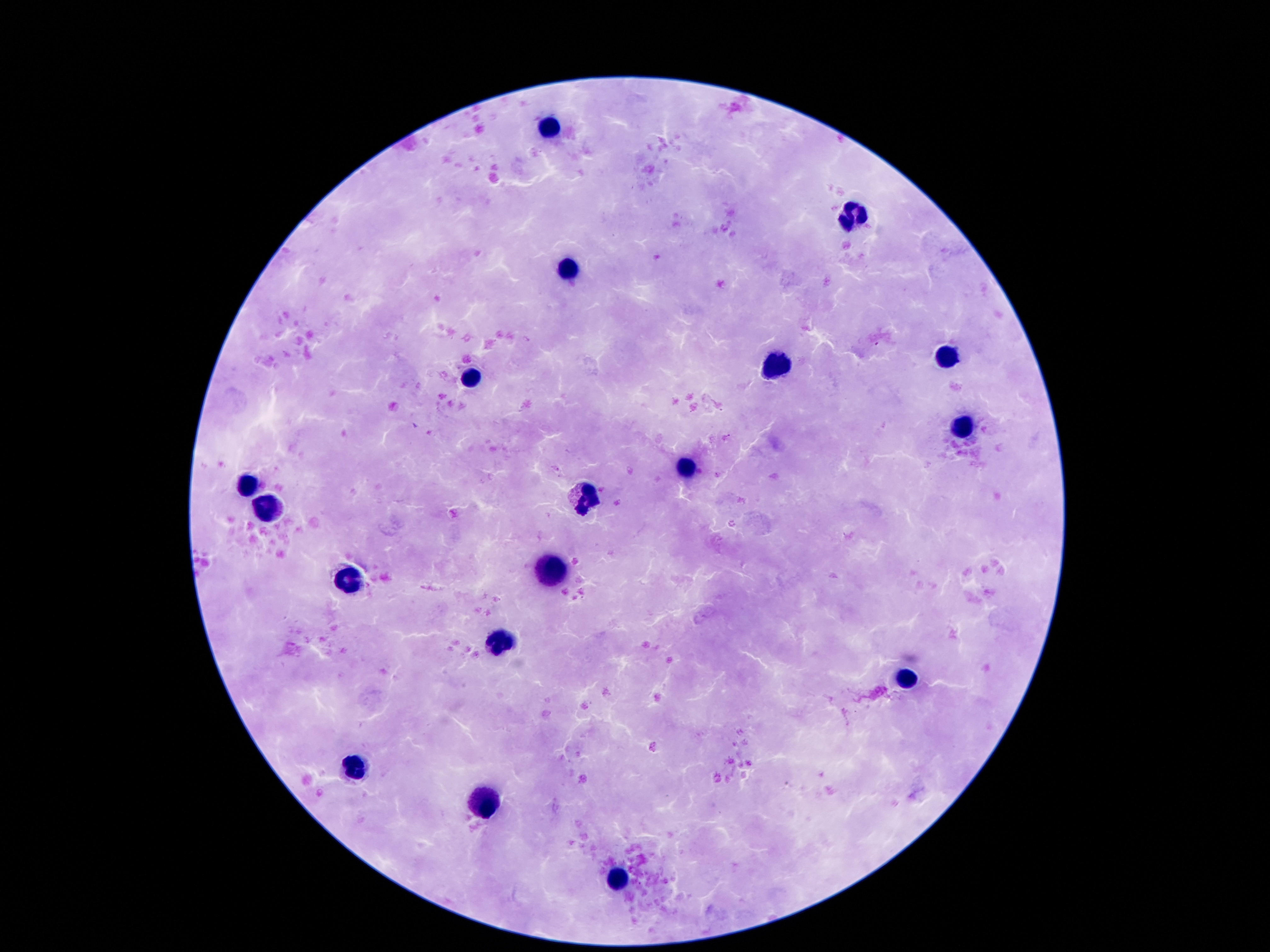

magnification = 100x
preparation = thick blood smear
leukocyte locations = approximate centers as {x, y} in pixels: {547, 125}, {853, 218}, {569, 268}, {947, 355}, {777, 367}, {471, 379}, {958, 426}, {688, 467}, {248, 486}, {585, 498}, {266, 510}, {548, 572}, {350, 584}, {500, 643}, {906, 676}, {355, 767}, {486, 805}, {617, 877}
patient malaria status = uninfected
capture = smartphone camera through the microscope eyepiece
stain = Giemsa
field of view = one from this slide
image size = 1270×952 pixels